Locate platelets.
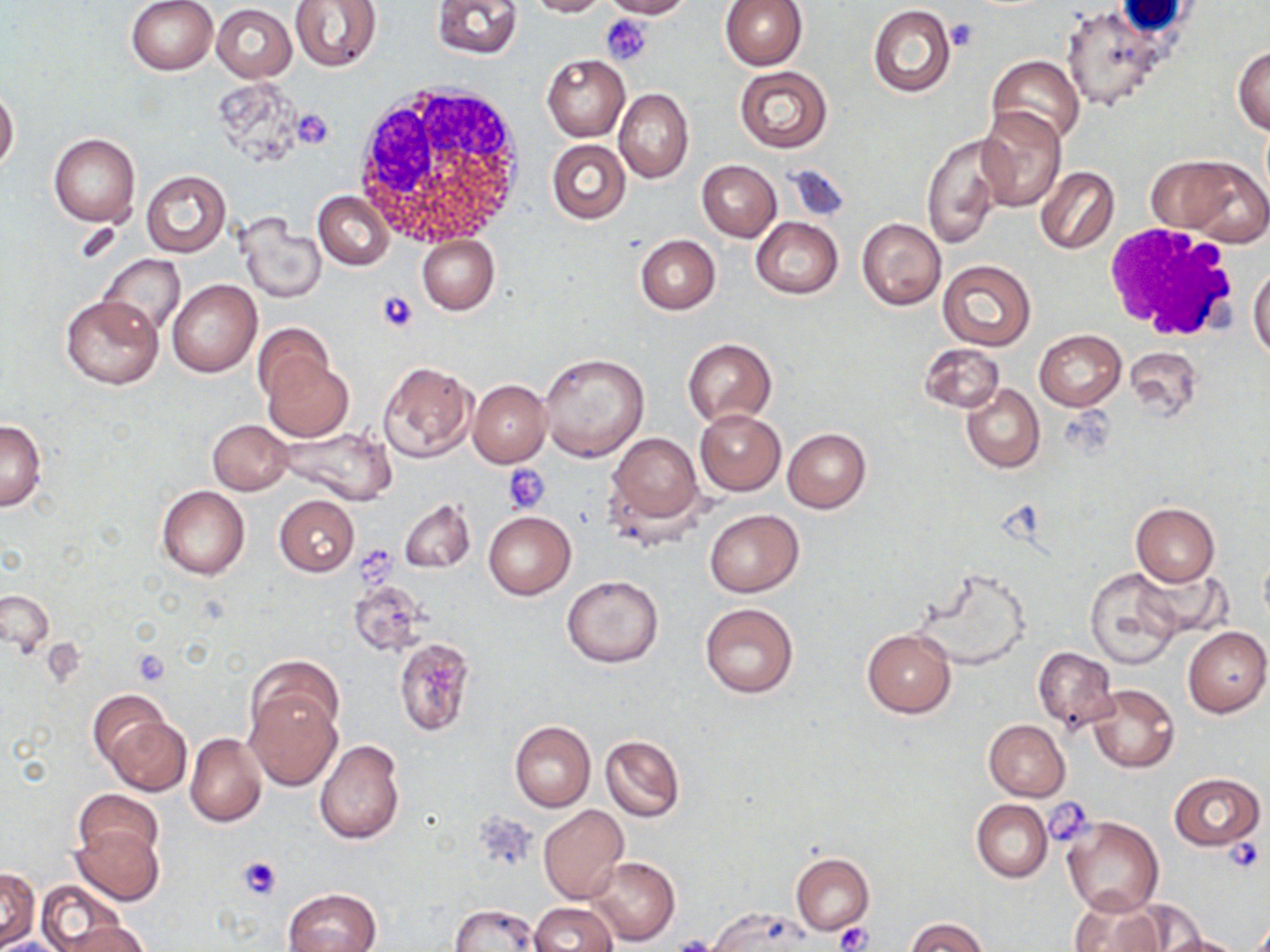
Approximate bounding boxes as (x1,y1)-(x2,y2) corner pairs in pixels.
Platelets: (601,14)-(652,66), (946,19)-(979,51), (291,110)-(335,149), (376,289)-(419,334), (504,464)-(552,513), (356,549)-(400,587), (43,640)-(85,684), (131,648)-(170,685), (1045,799)-(1095,844), (472,813)-(538,873), (1222,836)-(1264,876), (237,855)-(281,899), (835,922)-(872,952), (670,935)-(722,952).

Summary:
  - Uninfected red blood cell locations: (125,0)-(218,75), (291,0)-(383,72), (431,0)-(522,59), (525,0)-(608,17), (598,0)-(691,18), (721,1)-(807,70), (212,4)-(297,81), (1062,4)-(1165,112), (868,5)-(955,98), (1234,46)-(1270,135), (542,54)-(630,141), (987,54)-(1085,147), (734,65)-(833,152), (0,87)-(19,173), (615,88)-(694,184), (977,107)-(1066,212), (49,133)-(140,226), (922,135)-(1004,249), (547,139)-(630,225), (1149,152)-(1269,244), (696,160)-(782,241), (783,163)-(851,223), (1033,167)-(1119,255), (141,170)-(231,257), (313,190)-(394,270), (857,217)-(946,311), (238,218)-(326,303), (751,218)-(842,299), (416,234)-(499,314), (635,235)-(720,314), (97,254)-(186,338), (938,260)-(1036,351), (1249,263)-(1270,361), (167,278)-(262,378), (61,295)-(163,390), (252,323)-(336,406), (1034,330)-(1126,411), (684,337)-(776,425), (919,342)-(1004,412), (1127,345)-(1205,422), (538,352)-(650,461), (262,355)-(354,442), (377,360)-(477,462), (468,380)-(551,467), (961,383)-(1044,473), (695,407)-(786,496), (207,419)-(291,495), (0,420)-(46,512), (277,424)-(399,505), (783,429)-(872,513), (608,433)-(704,524), (156,486)-(250,580), (274,495)-(359,577), (398,497)-(476,574), (1131,502)-(1220,587), (704,509)-(804,596), (482,511)-(575,600), (912,564)-(1032,666), (1135,565)-(1226,640), (1084,567)-(1184,669), (562,576)-(664,667), (346,578)-(430,659), (2,589)-(55,658), (700,603)-(798,699), (1182,626)-(1270,717), (862,628)-(955,717), (394,636)-(477,736), (1033,647)-(1116,731), (249,656)-(343,743), (1086,684)-(1178,773), (244,689)-(341,790), (88,691)-(173,767), (107,713)-(191,796), (983,719)-(1070,800), (509,721)-(595,811), (185,733)-(266,826), (600,734)-(685,823), (314,740)-(405,844), (1168,772)-(1265,850), (74,789)-(163,864), (971,799)-(1052,882), (538,805)-(628,902), (1064,817)-(1164,917), (69,825)-(164,907), (791,851)-(873,936), (587,856)-(678,945), (0,868)-(40,948), (36,880)-(128,952), (284,887)-(382,952), (1067,892)-(1167,952), (529,902)-(618,952), (448,903)-(542,952), (708,907)-(820,951), (907,918)-(989,952), (55,921)-(151,952), (1155,932)-(1247,952)
  - White blood cell locations: (350,80)-(529,251), (1107,219)-(1241,344)
  - Slide-level diagnosis: negative for blood parasites
  - Preparation: thin blood film
  - Magnification: 1000x
  - Image size: 1270×952 pixels
  - Field of view: one of a larger specimen
  - Modality: light microscopy
  - Stain: May-Grünwald-Giemsa